Give the position of every leukocyte visible.
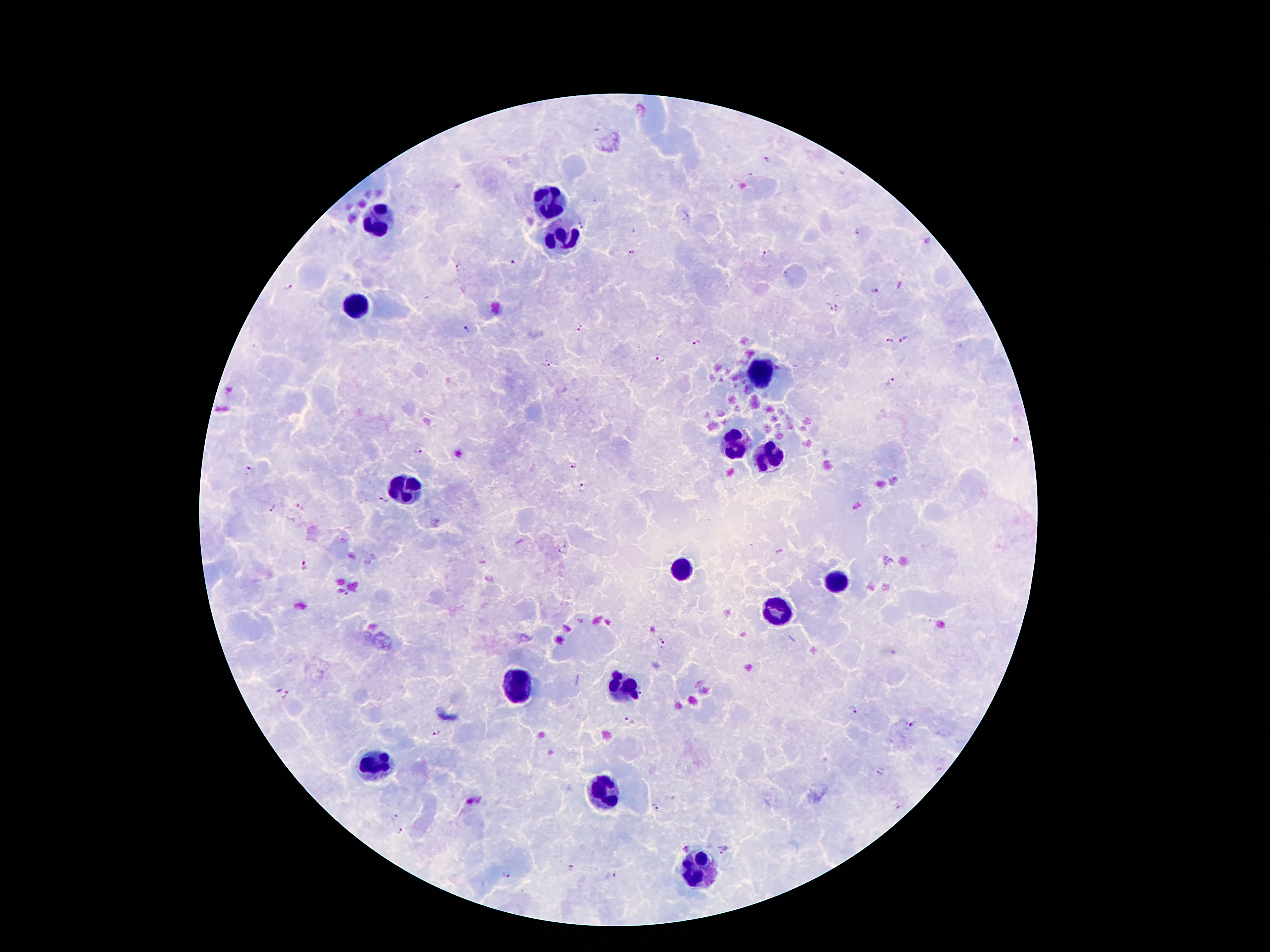
Approximate centers as {x, y} in pixels.
Leukocytes: {551, 202}, {376, 218}, {558, 237}, {354, 305}, {761, 367}, {730, 442}, {770, 454}, {409, 487}, {681, 566}, {836, 578}, {779, 610}, {516, 687}, {618, 688}, {374, 762}, {607, 785}, {700, 869}.

Malaria parasite locations: {582, 225}, {632, 251}, {766, 254}, {513, 261}, {459, 269}, {289, 287}, {876, 291}, {835, 310}, {579, 324}, {467, 329}, {905, 340}, {890, 341}, {697, 344}, {659, 357}, {546, 364}, {893, 383}, {419, 450}, {573, 468}, {248, 471}, {582, 488}, {383, 501}, {273, 509}, {563, 548}, {305, 566}, {662, 643}, {644, 689}, {287, 697}, {854, 709}, {630, 721}, {911, 724}, {437, 731}, {881, 771}, {657, 808}, {395, 817}, {401, 831}, {687, 849}, {723, 849}, {505, 876}, {610, 877}. Photographed through the microscope eyepiece with a smartphone camera. Image is 1270×952 pixels. One field from this slide. Thick peripheral-blood smear. Patient malaria status: positive for Plasmodium falciparum. 100x magnification. Giemsa stain.